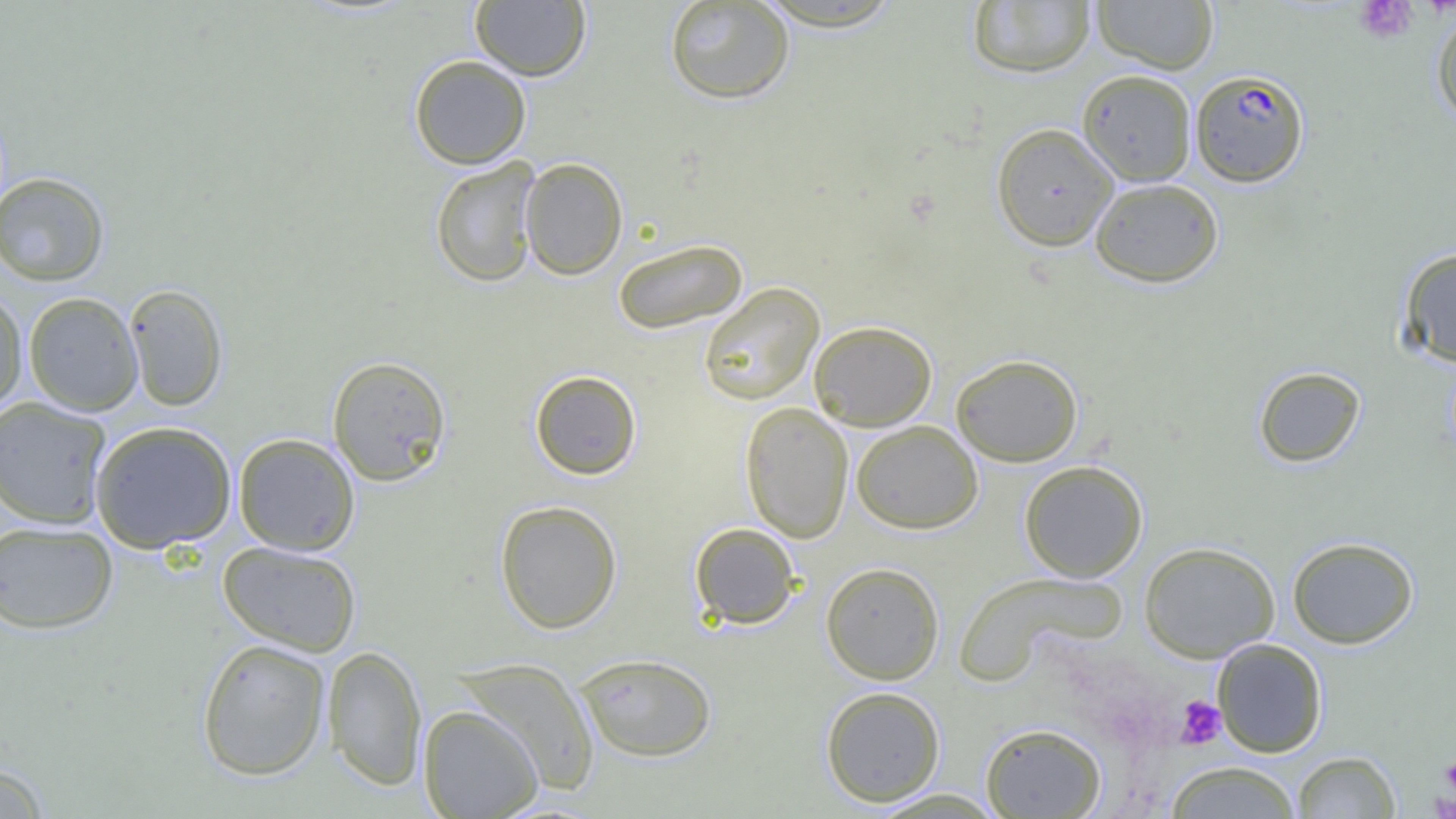
Summary:
  - Coordinate format: approximate bounding boxes as named x1/y1/x2/y2 corners in pixels
  - Plasmodium falciparum-infected red blood cell locations: (x1=1189, y1=69, x2=1309, y2=187)
  - Platelet locations: (x1=1354, y1=0, x2=1417, y2=43), (x1=1175, y1=696, x2=1226, y2=749), (x1=1441, y1=754, x2=1456, y2=795), (x1=1427, y1=790, x2=1455, y2=818)
  - Uninfected red blood cell locations: (x1=664, y1=0, x2=795, y2=105), (x1=1092, y1=0, x2=1218, y2=74), (x1=470, y1=1, x2=591, y2=80), (x1=752, y1=1, x2=906, y2=31), (x1=967, y1=1, x2=1096, y2=77), (x1=1431, y1=6, x2=1456, y2=126), (x1=409, y1=55, x2=531, y2=169), (x1=1077, y1=69, x2=1196, y2=186), (x1=991, y1=123, x2=1119, y2=251), (x1=429, y1=157, x2=542, y2=288), (x1=519, y1=157, x2=628, y2=280), (x1=0, y1=172, x2=110, y2=286), (x1=1089, y1=178, x2=1224, y2=288), (x1=612, y1=237, x2=748, y2=335), (x1=1397, y1=247, x2=1456, y2=367), (x1=123, y1=283, x2=228, y2=412), (x1=698, y1=283, x2=824, y2=405), (x1=0, y1=288, x2=28, y2=415), (x1=23, y1=292, x2=143, y2=416), (x1=808, y1=320, x2=937, y2=431), (x1=951, y1=354, x2=1083, y2=467), (x1=327, y1=355, x2=452, y2=486), (x1=1253, y1=365, x2=1366, y2=468), (x1=529, y1=370, x2=642, y2=479), (x1=0, y1=396, x2=113, y2=529), (x1=740, y1=401, x2=854, y2=543), (x1=90, y1=420, x2=238, y2=553), (x1=851, y1=420, x2=983, y2=534), (x1=233, y1=433, x2=360, y2=556), (x1=1018, y1=460, x2=1148, y2=582), (x1=494, y1=500, x2=623, y2=634), (x1=0, y1=520, x2=118, y2=634), (x1=689, y1=522, x2=801, y2=629), (x1=1287, y1=536, x2=1419, y2=649), (x1=217, y1=541, x2=362, y2=656), (x1=1138, y1=541, x2=1280, y2=662), (x1=821, y1=561, x2=945, y2=684), (x1=953, y1=570, x2=1127, y2=683), (x1=196, y1=638, x2=332, y2=781), (x1=1212, y1=638, x2=1328, y2=758), (x1=322, y1=644, x2=427, y2=791), (x1=574, y1=653, x2=718, y2=762), (x1=454, y1=657, x2=601, y2=795), (x1=820, y1=685, x2=945, y2=807), (x1=418, y1=704, x2=542, y2=819), (x1=980, y1=723, x2=1106, y2=818), (x1=1292, y1=751, x2=1401, y2=818), (x1=0, y1=760, x2=53, y2=819), (x1=1162, y1=760, x2=1304, y2=818), (x1=865, y1=788, x2=1008, y2=818)
  - Slide-level diagnosis: Plasmodium falciparum
  - Magnification: 1000x
  - Image size: 1456×819 pixels
  - Modality: optical microscopy
  - Preparation: thin blood smear
  - Field of view: one of a larger specimen